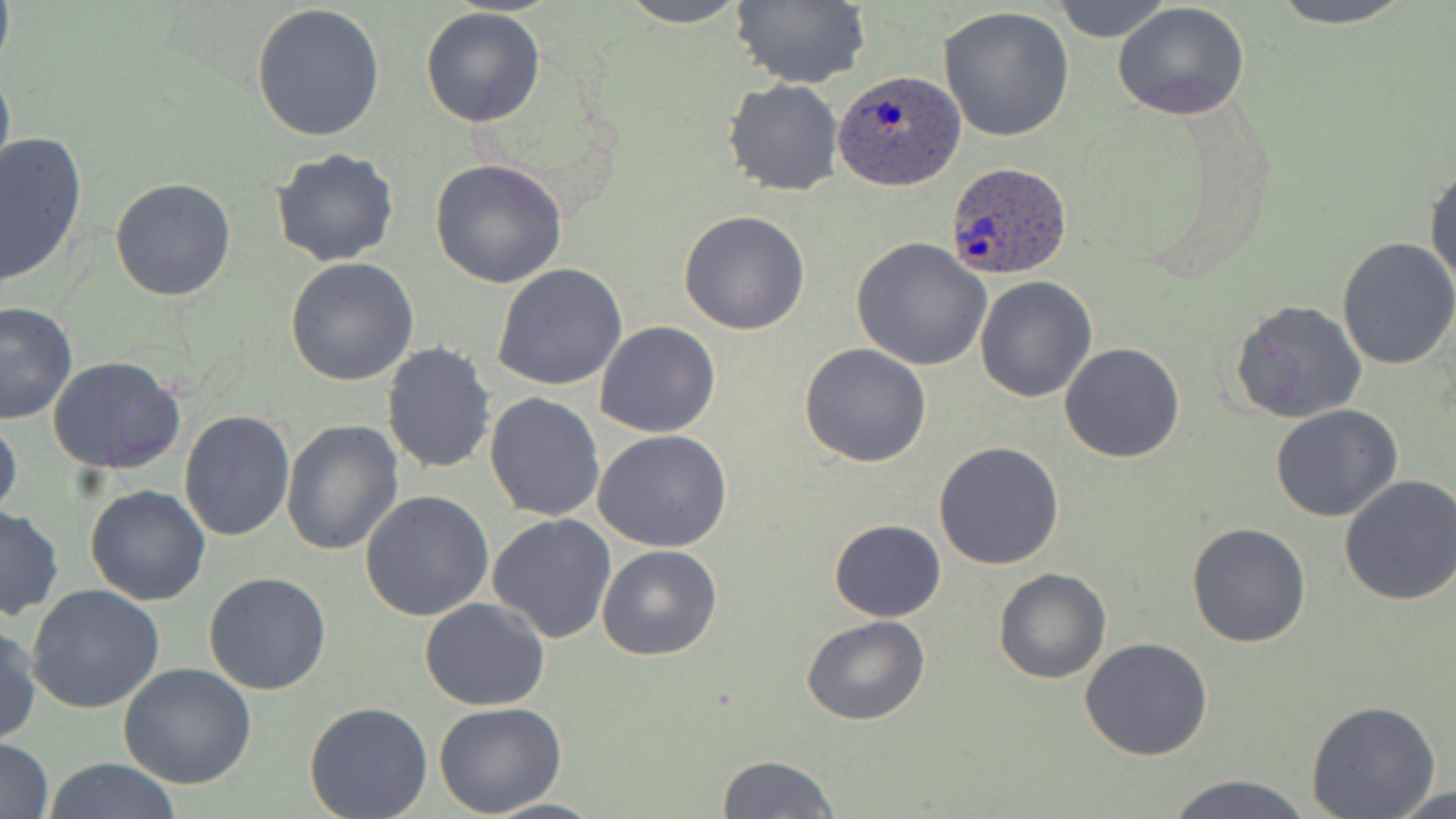

slide-level diagnosis = Plasmodium ovale
magnification = 1000x
modality = light microscopy
preparation = thin blood film
field of view = single
stain = May-Grünwald-Giemsa
image size = 1456×819 pixels
uninfected red blood cell locations = approximate bounding boxes as (x1,y1)-(x2,y2) corner pairs in pixels: (614,0)-(753,27), (730,0)-(870,90), (1050,0)-(1173,43), (1262,0)-(1420,28), (250,2)-(387,141), (1113,2)-(1250,121), (937,6)-(1077,142), (420,8)-(546,127), (0,62)-(14,188), (722,78)-(845,197), (1,133)-(88,290), (271,148)-(399,267), (429,158)-(568,288), (1425,164)-(1456,291), (109,177)-(236,301), (679,209)-(810,335), (1336,237)-(1456,372), (851,238)-(993,372), (284,258)-(419,387), (492,264)-(628,391), (975,275)-(1096,402), (1229,299)-(1366,424), (0,301)-(80,426), (594,321)-(722,438), (380,342)-(497,476), (799,342)-(930,467), (1059,342)-(1185,463), (48,355)-(185,477), (483,391)-(605,522), (1270,404)-(1403,522), (178,409)-(297,542), (0,412)-(22,524), (280,419)-(402,556), (593,429)-(734,552), (934,442)-(1065,571), (1338,475)-(1456,608), (85,484)-(212,605), (359,491)-(494,621), (0,505)-(65,622), (487,514)-(617,644), (829,519)-(946,621), (1187,523)-(1310,647), (596,544)-(723,662), (992,567)-(1111,685), (203,571)-(331,695), (26,586)-(166,714), (419,597)-(550,711), (801,614)-(931,726), (1,621)-(41,747), (1079,637)-(1213,760), (118,663)-(259,790), (1305,700)-(1441,818), (303,701)-(433,819), (433,702)-(567,818), (0,737)-(53,819), (716,755)-(840,818), (42,759)-(184,819), (1162,774)-(1317,819), (1383,783)-(1456,819), (480,796)-(608,818)
Plasmodium ovale-infected red blood cell locations = approximate bounding boxes as (x1,y1)-(x2,y2) corner pairs in pixels: (834,71)-(967,192), (946,161)-(1071,281)